Comment on the morphology of the red blood cells.
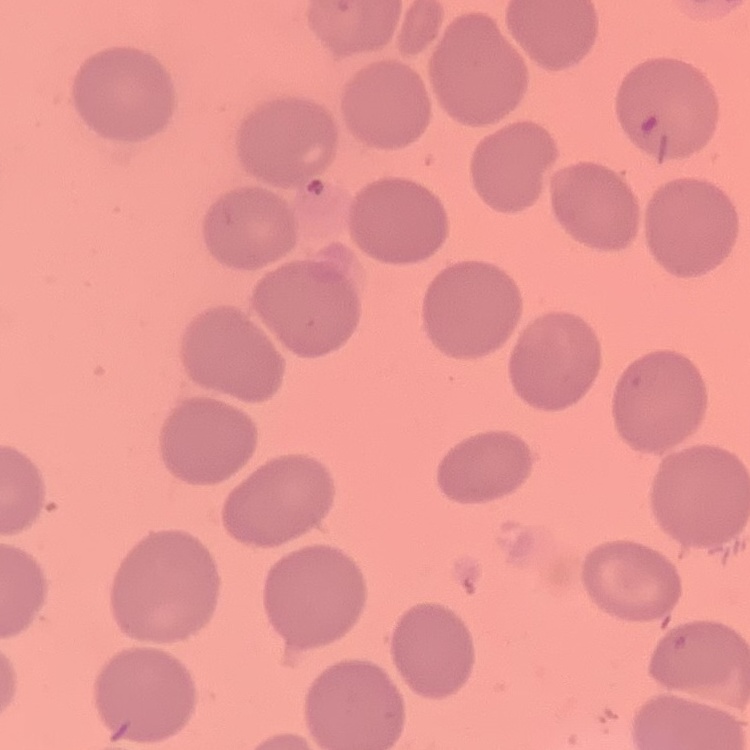
No rouleaux formation.

image type = one tile cut from a larger photomicrograph
preparation = thin peripheral smear
stain = Field's or Giemsa